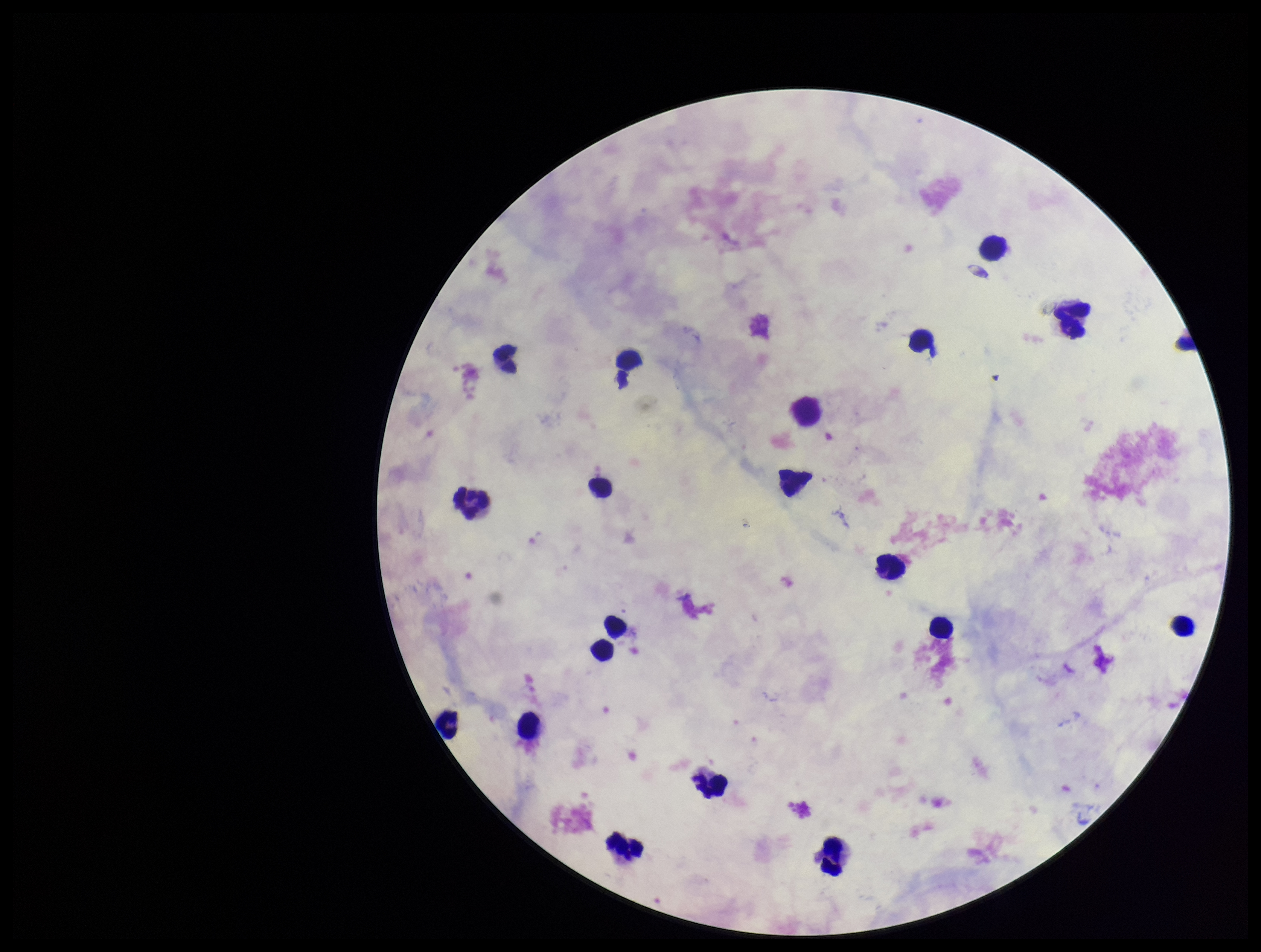
Preparation: thick smear. Parasite count: 0. Photographed through the microscope eyepiece with a smartphone camera. Leukocyte count: 18. Image is 1261×952 pixels. One field from this slide. Patient malaria status: negative. Stained with Giemsa. Plasmodium parasites: none detected.